Assess the morphology of the red blood cells.
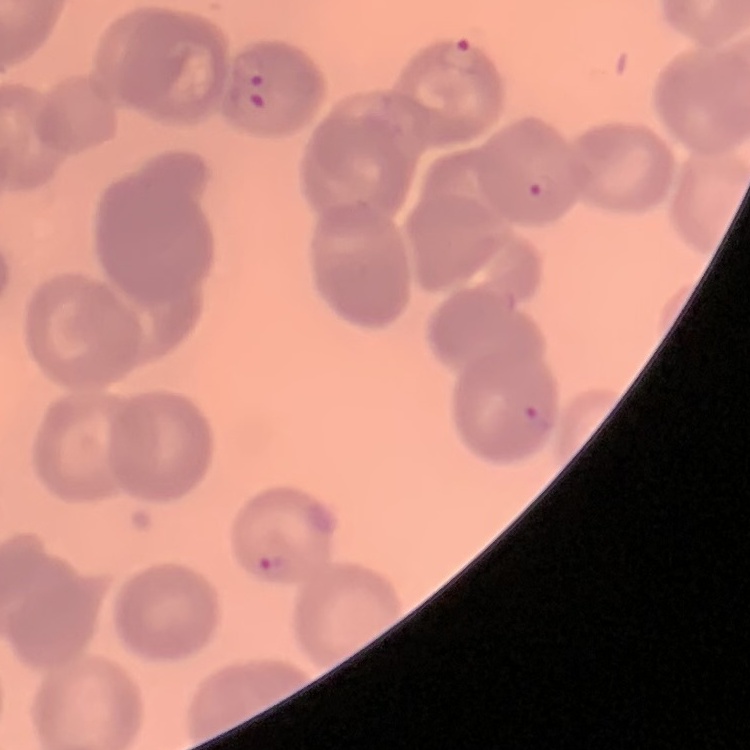

No rouleaux formation.

Thin blood smear. One tile cut from a larger photomicrograph. Stained with either Field's or Giemsa.